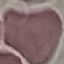

Summary:
  - Malaria status: uninfected
  - Preparation: thin smear
  - Capture: smartphone camera at the microscope eyepiece
  - Stain: Giemsa
  - Image type: automatically extracted cell patch, resized to 64 × 64 pixels